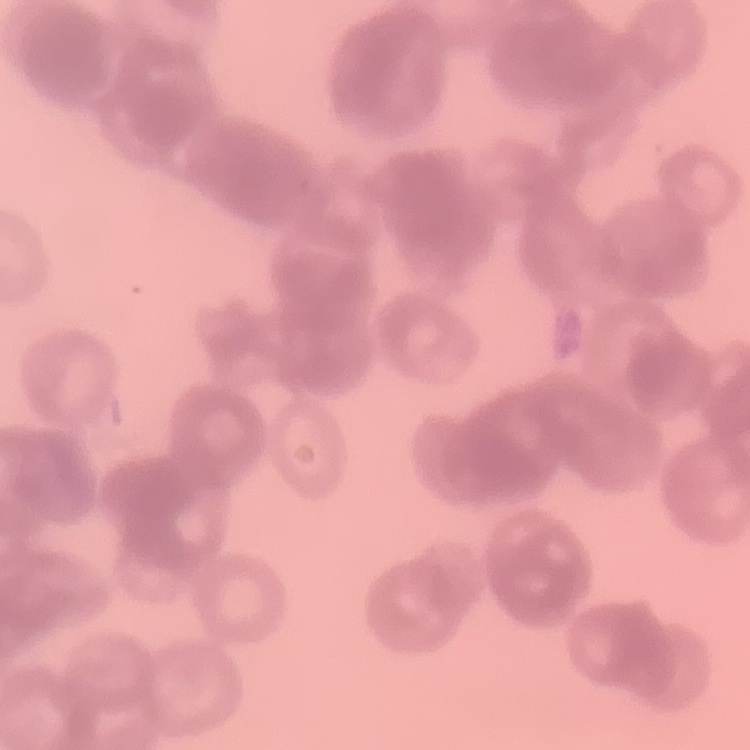

The erythrocytes show rouleaux formation. Thin peripheral smear. Square crop of a larger photomicrograph. Stained with either Field's or Giemsa.